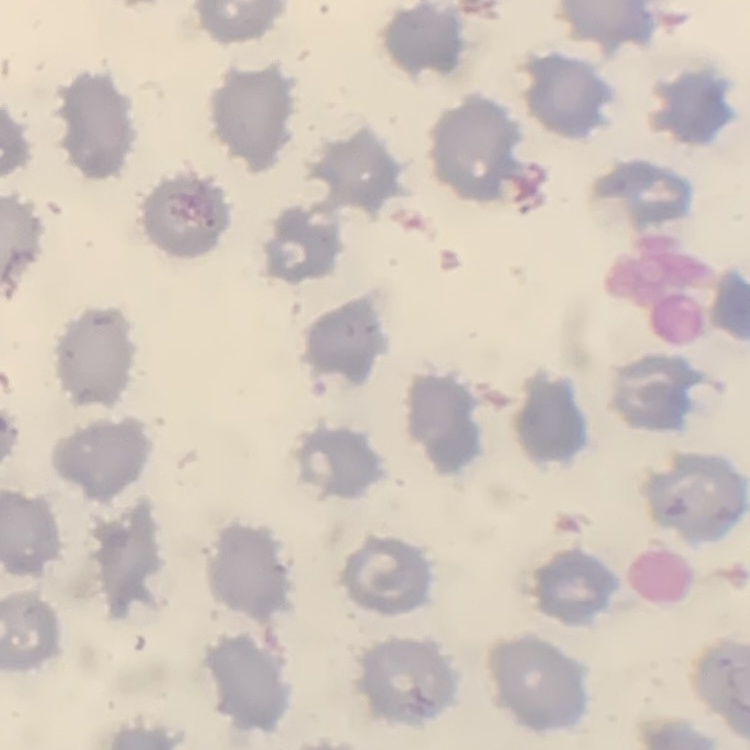

The erythrocytes show no rouleaux formation. Thin blood film. Field's or Giemsa stain. Square crop of a larger photomicrograph.